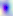
Summary:
  - Modality: micrograph
  - Magnification: 400x
  - Identification: Toxoplasma gondii